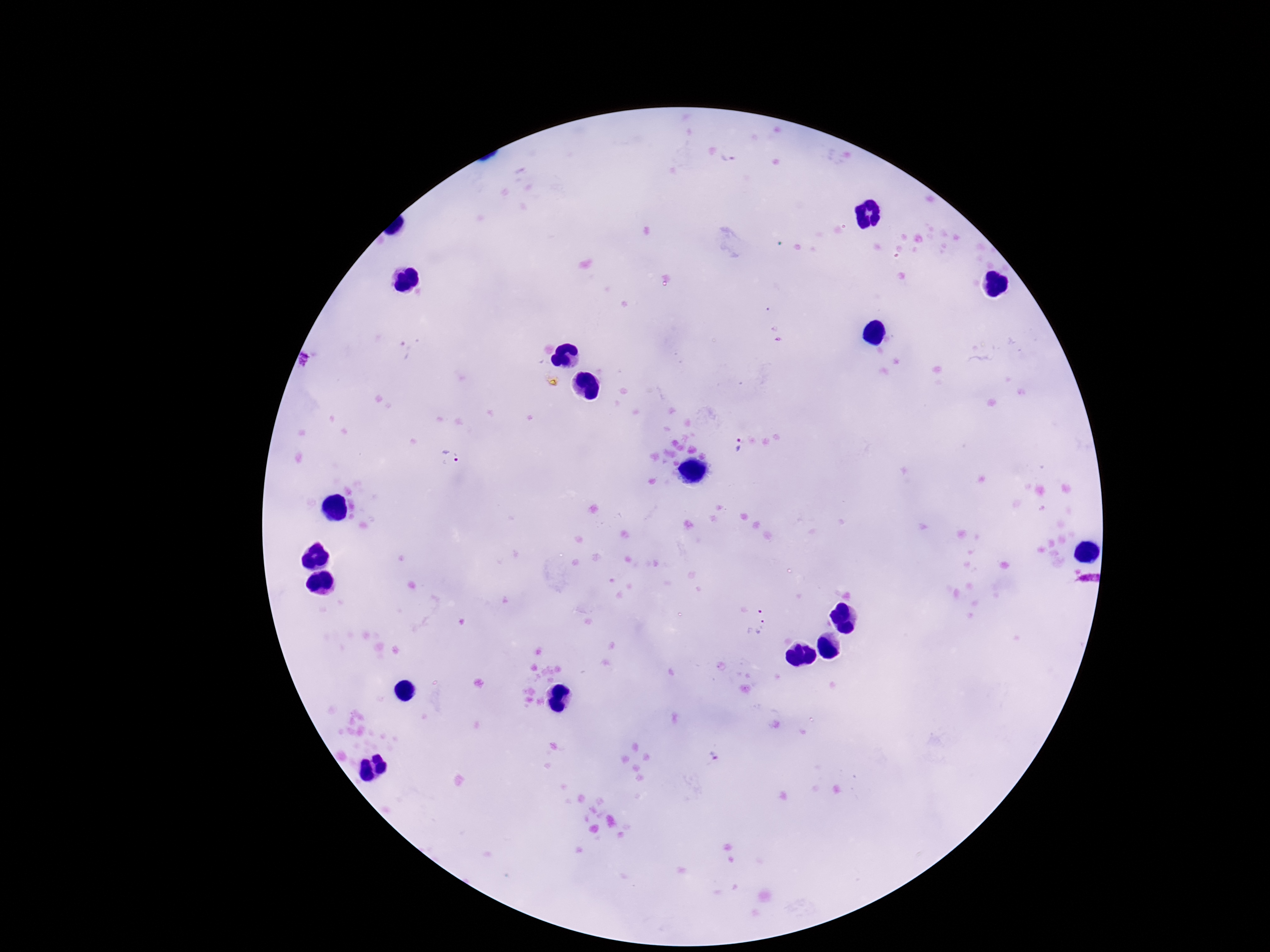 Approximate object centers, in pixels from the top-left corner. Plasmodium parasite locations: (x=737, y=444), (x=450, y=458), (x=752, y=605), (x=758, y=629), (x=711, y=759). Image is 1270×952 pixels. Thick blood film. Giemsa stain. Patient malaria status: positive. 100x magnification. Smartphone photograph taken through the microscope eyepiece. Single field of view.